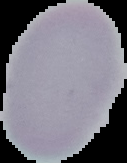
From a thin blood smear. Malaria status: uninfected. Image is 127×163 pixels. Segmented cell region on a black background.